Report the malaria status.
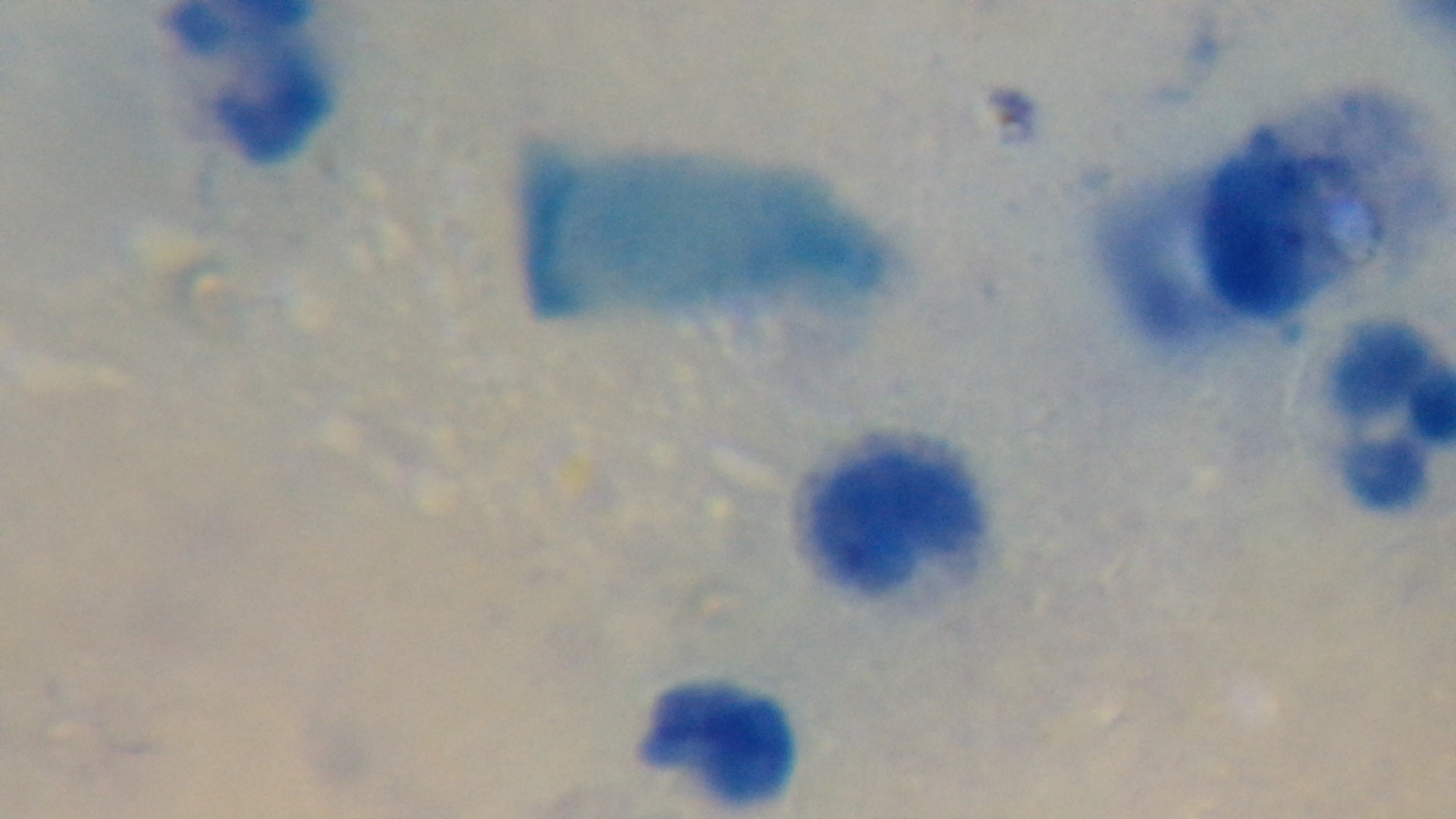

Uninfected.

stain = Giemsa
objective = 100x oil immersion
field of view = one from the slide
preparation = thick blood film
capture = mounted 4K digital camera
modality = light microscopy